Look for Plasmodium parasites.
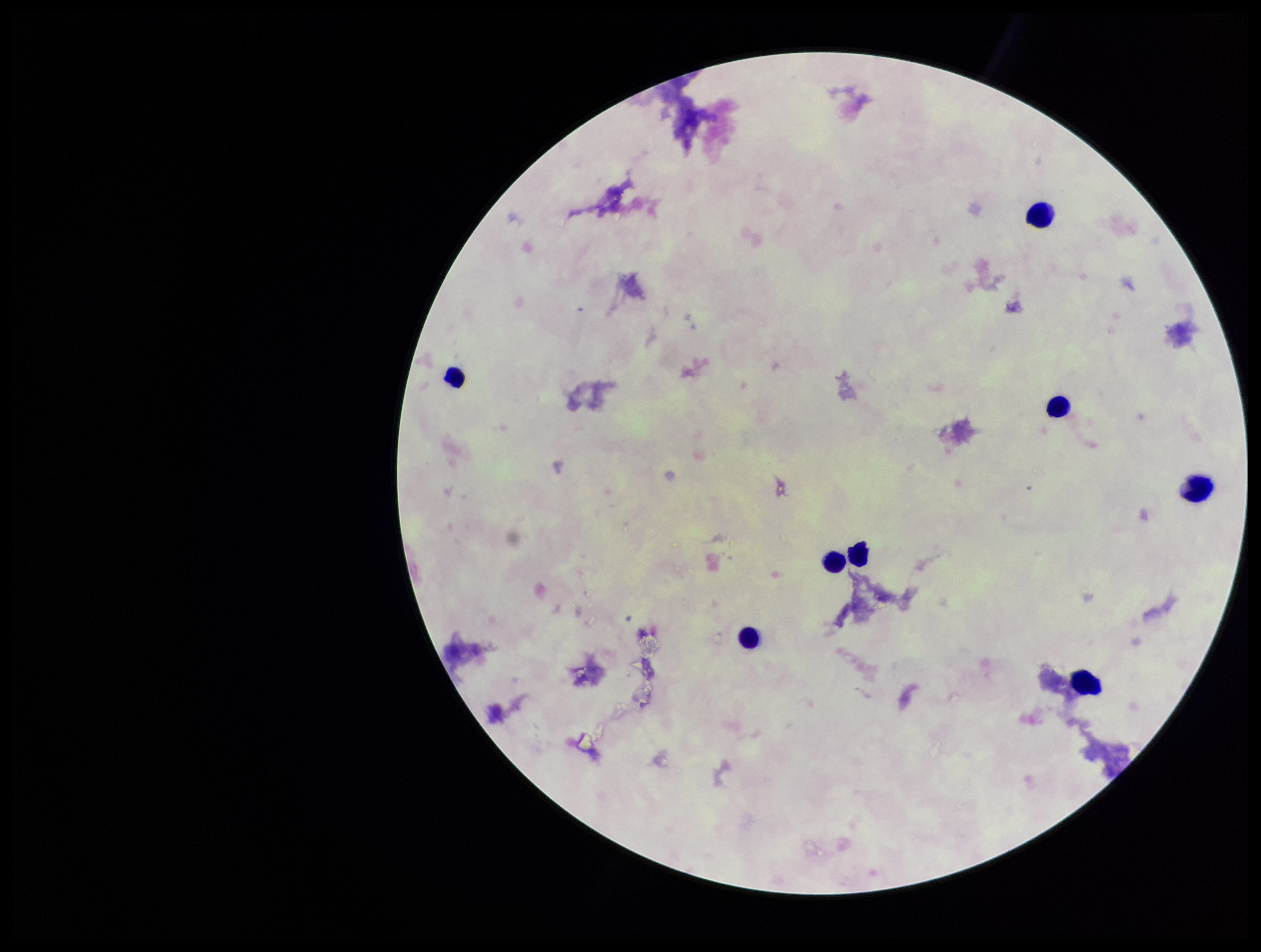
None detected.

field of view = one from this slide
leukocyte count = 8
preparation = thick
capture = smartphone photograph through the microscope eyepiece
image size = 1261×952 pixels
stain = Giemsa
patient malaria status = negative
parasite count = 0